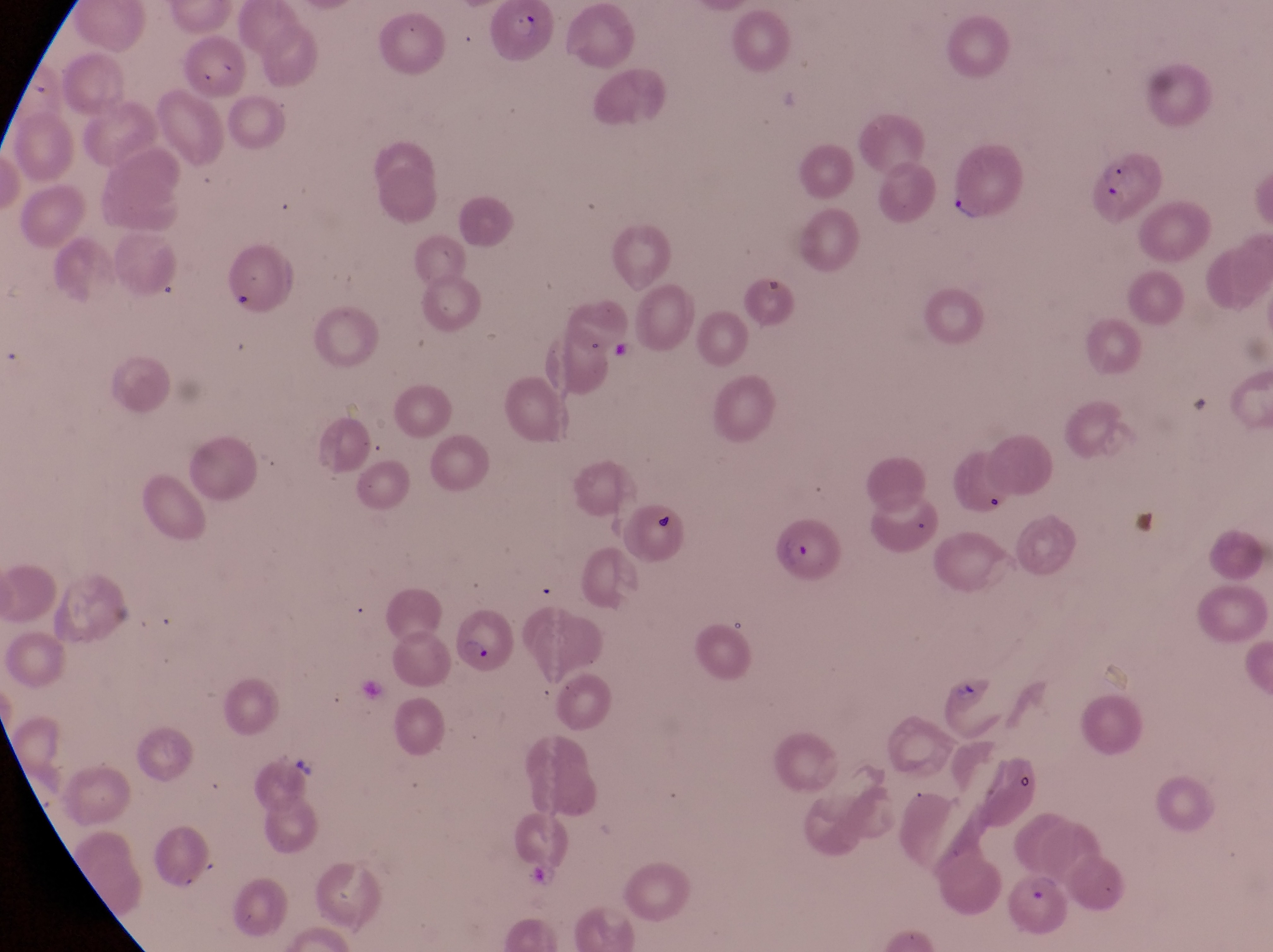 Approximate bounding boxes as {left, top, right, bottom} in pixels. Parasitised red blood cell locations: {486, 3, 556, 73}, {936, 147, 1024, 224}, {766, 515, 841, 583}, {451, 600, 514, 675}, {1016, 873, 1077, 940}. Artifact (platelet-like body, stain precipitate, or debris) locations: {218, 280, 253, 312}, {609, 340, 641, 370}, {647, 512, 677, 537}. Thin blood smear. At a magnification of 1000x. Single field of view. Image is 1273×952 pixels. Collected in Uganda. Photographed through the eyepiece of an Olympus CX-23 microscope with a smartphone camera.